Give the extent of all uninfected red blood cells.
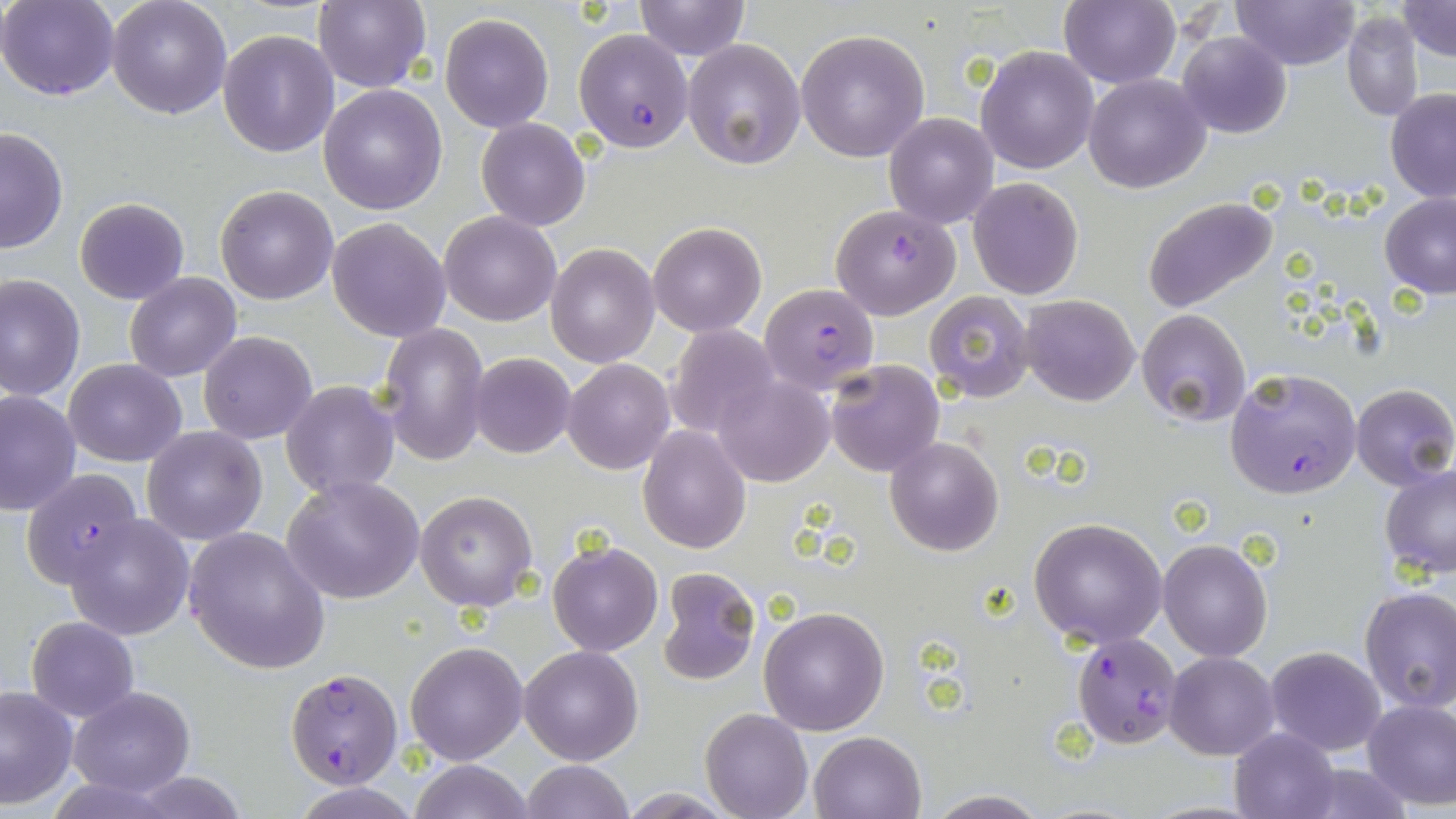

Approximate bounding boxes as (x1, y1, x2, y2) in pixels.
Uninfected red blood cells: (1, 0, 120, 101), (107, 0, 232, 119), (314, 0, 432, 93), (634, 0, 749, 60), (1060, 0, 1181, 89), (1232, 0, 1361, 70), (1396, 0, 1455, 62), (1342, 12, 1424, 122), (440, 13, 554, 131), (796, 28, 931, 162), (219, 30, 339, 157), (1176, 30, 1292, 138), (682, 39, 806, 172), (976, 45, 1098, 174), (1083, 72, 1211, 193), (319, 83, 449, 214), (1386, 88, 1456, 201), (884, 113, 998, 228), (476, 117, 591, 232), (0, 126, 69, 253), (967, 177, 1084, 300), (214, 184, 338, 304), (1379, 193, 1456, 299), (74, 197, 189, 305), (1142, 197, 1279, 315), (440, 212, 562, 327), (326, 218, 451, 341), (647, 220, 766, 336), (547, 243, 660, 367), (125, 271, 241, 382), (0, 273, 86, 404), (923, 290, 1036, 404), (1020, 294, 1140, 406), (1136, 309, 1251, 426), (377, 321, 490, 465), (665, 325, 780, 440), (199, 330, 317, 445), (469, 353, 574, 457), (65, 358, 185, 467), (563, 358, 674, 474), (824, 358, 944, 476), (712, 374, 835, 487), (281, 382, 398, 498), (1351, 384, 1455, 491), (0, 389, 80, 517), (639, 423, 750, 552), (141, 426, 267, 546), (885, 437, 1004, 556), (1380, 465, 1456, 580), (283, 477, 425, 605), (415, 490, 538, 612), (64, 513, 193, 639), (1028, 516, 1168, 647), (184, 527, 331, 674), (1159, 538, 1272, 661), (548, 540, 663, 656), (655, 566, 762, 686), (1357, 587, 1456, 714), (758, 605, 890, 736), (27, 616, 138, 723), (406, 642, 528, 765), (520, 644, 641, 764), (1264, 646, 1387, 755), (1165, 650, 1280, 760), (0, 686, 76, 809), (67, 686, 195, 798), (1362, 697, 1456, 810), (700, 707, 813, 819), (1228, 727, 1342, 819), (809, 730, 927, 819), (408, 759, 531, 819), (520, 760, 634, 818), (294, 783, 420, 818), (615, 789, 740, 818), (923, 791, 1051, 819).

Summary:
  - Plasmodium falciparum-infected red blood cell locations: (575, 28, 692, 152), (830, 203, 961, 319), (760, 284, 879, 395), (1226, 368, 1363, 499), (17, 468, 147, 588), (1070, 632, 1182, 749), (285, 667, 401, 788)
  - Slide-level diagnosis: Plasmodium falciparum
  - Modality: optical microscopy
  - Field of view: single
  - Image size: 1456×819 pixels
  - Preparation: thin blood smear
  - Magnification: 1000x
  - Stain: May-Grünwald-Giemsa